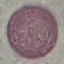

malaria status = uninfected
preparation = thin blood smear
stain = Giemsa
image type = cell patch, automatically extracted from a larger field of view and resized to 64 × 64 pixels
capture = smartphone through the microscope eyepiece